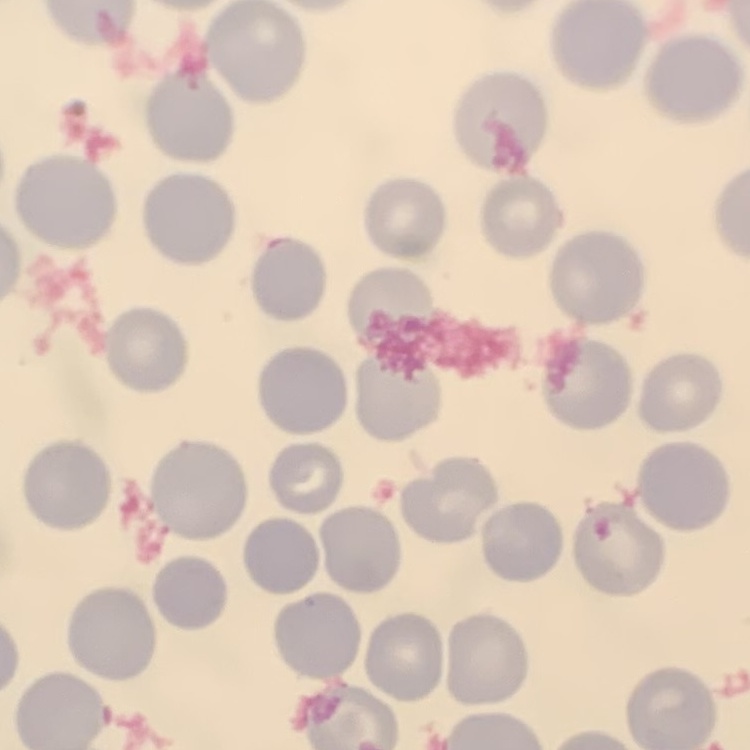

erythrocyte_morphology: no rouleaux formation
preparation: thin blood film
stain: Field's or Giemsa
image_type: one tile cut from a larger photomicrograph